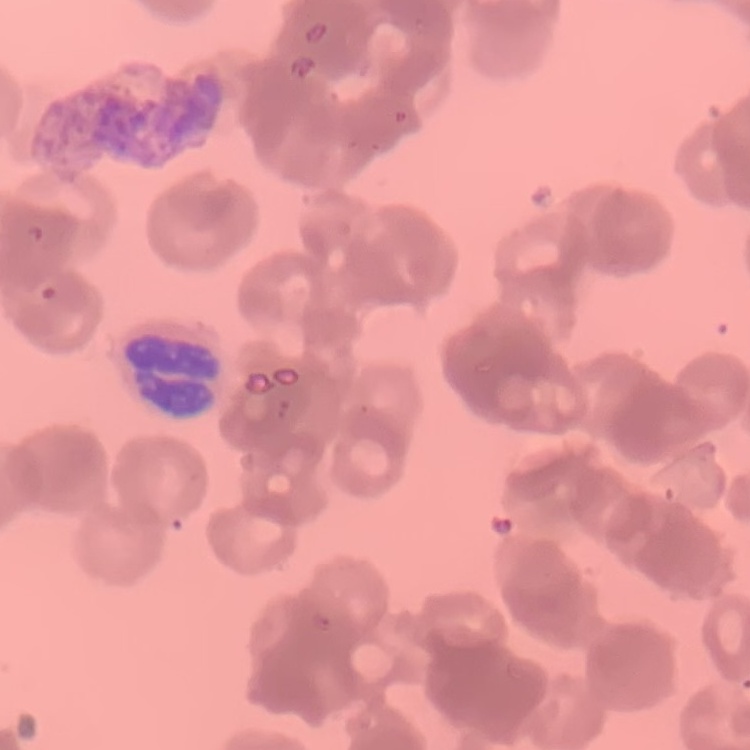
The red blood cells exhibit rouleaux formation. Square crop of a larger photomicrograph. Thin blood film. Field's or Giemsa stain.